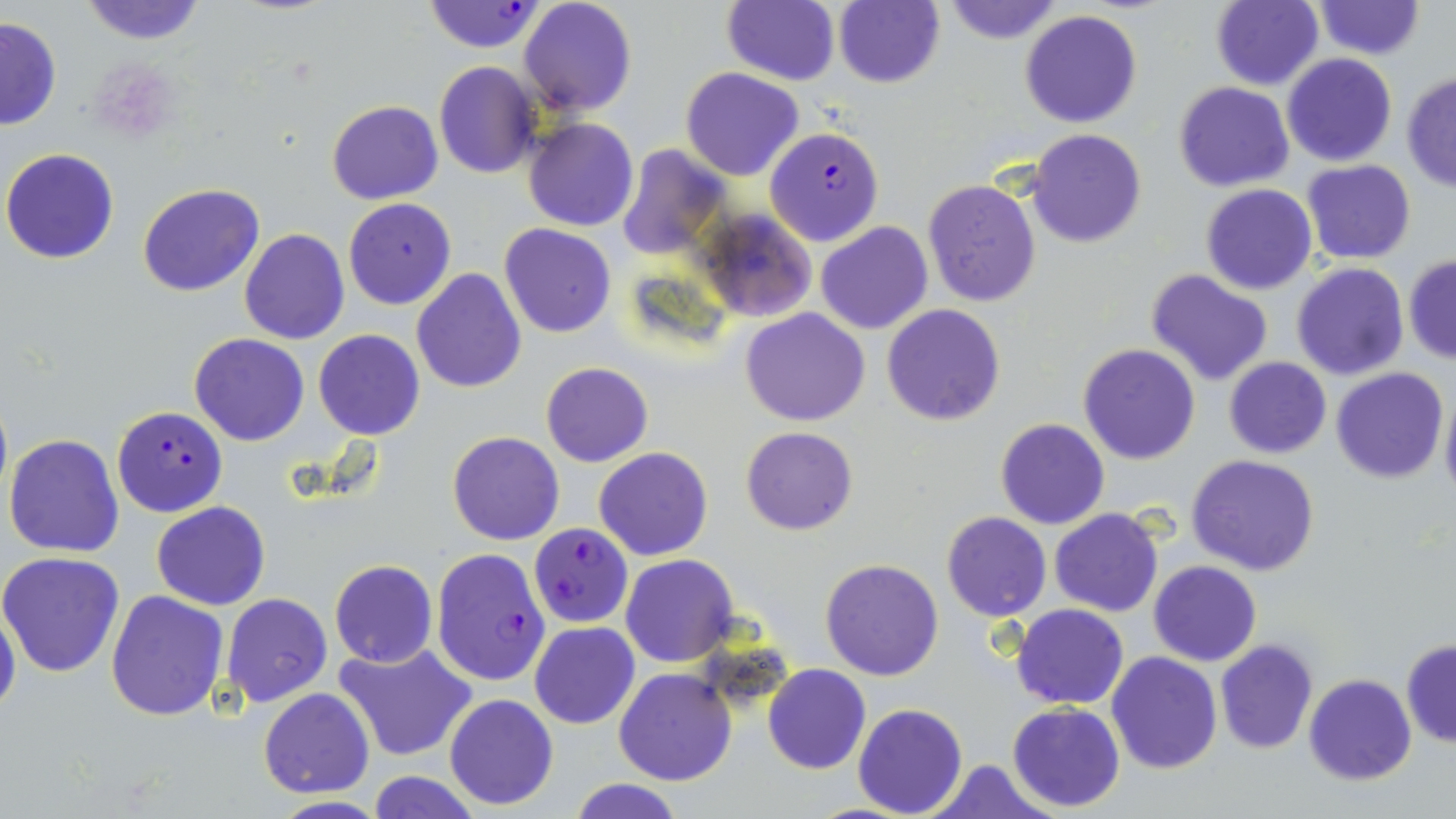
slide-level diagnosis = Plasmodium falciparum
magnification = 1000x
stain = May-Grünwald-Giemsa
modality = optical microscopy
preparation = thin blood smear
Plasmodium falciparum-infected red blood cell locations = approximate bounding boxes as named x1/y1/x2/y2 corners in pixels: (x1=425, y1=1, x2=544, y2=52), (x1=764, y1=126, x2=885, y2=246), (x1=112, y1=406, x2=228, y2=517), (x1=529, y1=523, x2=632, y2=629), (x1=430, y1=548, x2=551, y2=688)
image size = 1456×819 pixels
field of view = one of a larger specimen
uninfected red blood cell locations = approximate bounding boxes as named x1/y1/x2/y2 corners in pixels: (x1=78, y1=0, x2=208, y2=44), (x1=518, y1=0, x2=638, y2=117), (x1=945, y1=0, x2=1062, y2=45), (x1=1210, y1=0, x2=1323, y2=91), (x1=1314, y1=0, x2=1423, y2=59), (x1=721, y1=1, x2=840, y2=85), (x1=832, y1=1, x2=946, y2=88), (x1=1021, y1=10, x2=1143, y2=128), (x1=0, y1=13, x2=62, y2=133), (x1=1282, y1=53, x2=1396, y2=167), (x1=434, y1=62, x2=540, y2=178), (x1=680, y1=66, x2=803, y2=180), (x1=1401, y1=71, x2=1456, y2=191), (x1=1173, y1=81, x2=1295, y2=191), (x1=326, y1=100, x2=444, y2=205), (x1=523, y1=118, x2=638, y2=232), (x1=1028, y1=128, x2=1145, y2=248), (x1=616, y1=146, x2=729, y2=261), (x1=1, y1=148, x2=120, y2=264), (x1=1302, y1=161, x2=1416, y2=264), (x1=922, y1=177, x2=1041, y2=306), (x1=138, y1=183, x2=265, y2=297), (x1=1200, y1=184, x2=1318, y2=295), (x1=343, y1=197, x2=457, y2=310), (x1=697, y1=209, x2=818, y2=324), (x1=816, y1=221, x2=932, y2=335), (x1=378, y1=222, x2=506, y2=360), (x1=499, y1=223, x2=616, y2=338), (x1=240, y1=229, x2=349, y2=344), (x1=1404, y1=254, x2=1456, y2=364), (x1=1293, y1=263, x2=1408, y2=381), (x1=410, y1=267, x2=526, y2=394), (x1=1145, y1=267, x2=1275, y2=387), (x1=882, y1=303, x2=1004, y2=426), (x1=740, y1=308, x2=871, y2=426), (x1=313, y1=330, x2=424, y2=441), (x1=189, y1=333, x2=309, y2=446), (x1=1079, y1=344, x2=1200, y2=465), (x1=1224, y1=358, x2=1331, y2=458), (x1=541, y1=362, x2=652, y2=467), (x1=1333, y1=367, x2=1448, y2=483), (x1=1440, y1=387, x2=1456, y2=506), (x1=995, y1=419, x2=1109, y2=531), (x1=740, y1=425, x2=858, y2=534), (x1=447, y1=431, x2=564, y2=546), (x1=4, y1=433, x2=126, y2=557), (x1=594, y1=447, x2=713, y2=561), (x1=1187, y1=454, x2=1319, y2=575), (x1=152, y1=501, x2=270, y2=610), (x1=1050, y1=507, x2=1163, y2=617), (x1=941, y1=512, x2=1051, y2=621), (x1=0, y1=552, x2=127, y2=677), (x1=621, y1=553, x2=740, y2=667), (x1=329, y1=559, x2=437, y2=668), (x1=820, y1=559, x2=944, y2=681), (x1=1149, y1=561, x2=1260, y2=666), (x1=106, y1=589, x2=230, y2=722), (x1=222, y1=593, x2=332, y2=707), (x1=0, y1=596, x2=22, y2=724), (x1=1011, y1=604, x2=1128, y2=709), (x1=531, y1=623, x2=639, y2=729), (x1=1400, y1=639, x2=1456, y2=748), (x1=1215, y1=640, x2=1317, y2=754), (x1=333, y1=642, x2=481, y2=763), (x1=1106, y1=651, x2=1221, y2=773), (x1=763, y1=664, x2=871, y2=776), (x1=360, y1=667, x2=546, y2=794), (x1=614, y1=668, x2=737, y2=785), (x1=1303, y1=674, x2=1416, y2=785), (x1=258, y1=688, x2=374, y2=798), (x1=444, y1=693, x2=559, y2=809), (x1=853, y1=702, x2=968, y2=817), (x1=1007, y1=703, x2=1125, y2=812), (x1=930, y1=759, x2=1056, y2=818), (x1=365, y1=772, x2=482, y2=818), (x1=564, y1=778, x2=690, y2=818), (x1=261, y1=796, x2=394, y2=818)